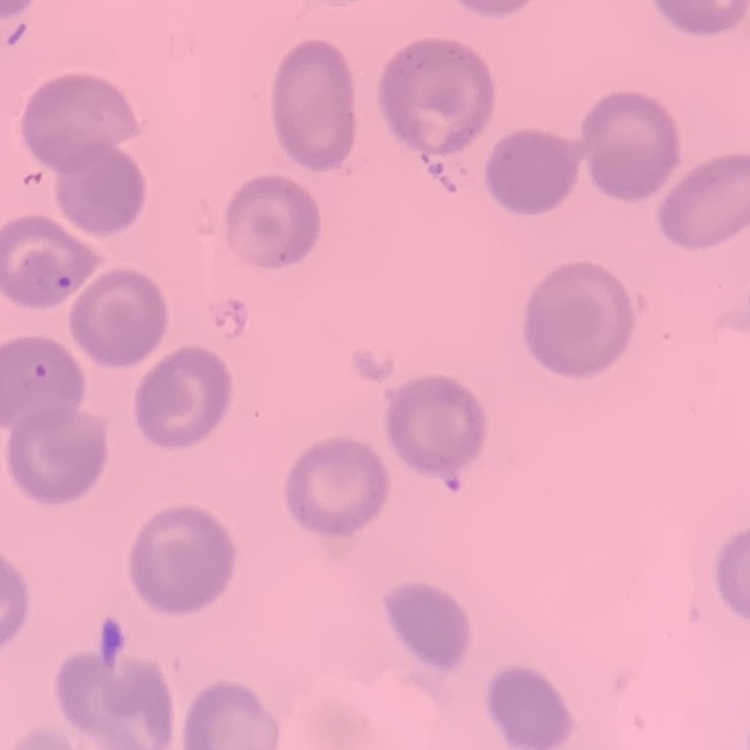
{
  "erythrocyte_morphology": "no rouleaux formation",
  "preparation": "thin blood smear",
  "stain": "Field's or Giemsa",
  "image_type": "square crop of a larger photomicrograph"
}